Outline each blood parasite and name the species.
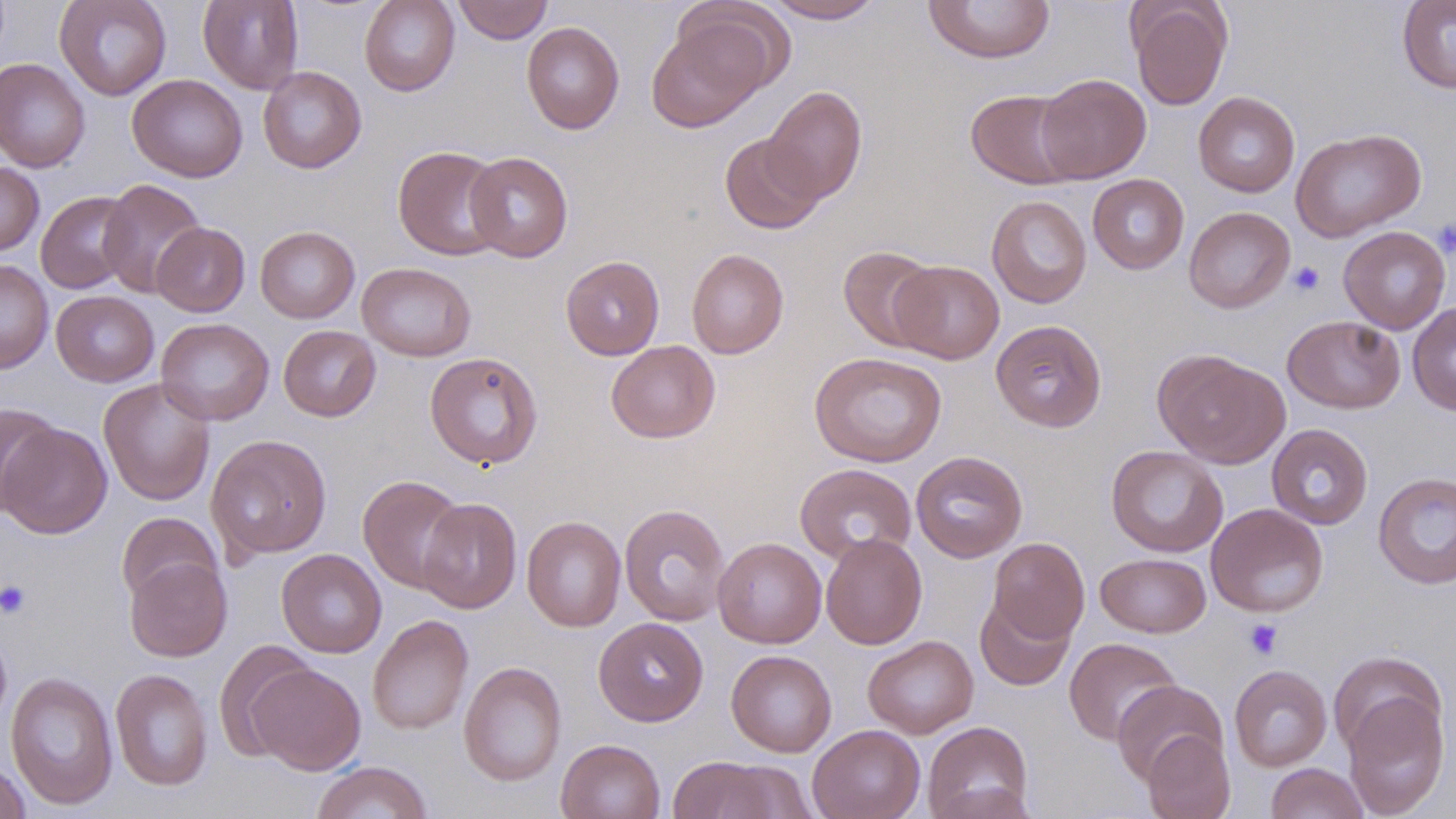
No blood parasites observed.

slide_level_diagnosis: no evidence of blood parasites
uninfected_red_blood_cell_locations: 'approximate bounding boxes as (x1,y1)-(x2,y2) corner pairs in pixels: (54,0)-(172,101), (198,0)-(304,94), (359,0)-(460,96), (453,0)-(553,44), (763,0)-(886,23), (1128,0)-(1233,110), (922,1)-(1055,65), (1397,1)-(1456,93), (646,18)-(770,132), (521,22)-(624,134), (0,58)-(90,173), (258,66)-(367,173), (127,74)-(247,182), (1035,74)-(1151,183), (762,85)-(867,204), (965,88)-(1083,189), (1193,91)-(1300,197), (1290,128)-(1426,242), (720,133)-(826,234), (392,145)-(507,261), (465,151)-(573,263), (0,161)-(44,256), (1088,174)-(1189,274), (98,179)-(206,298), (36,191)-(136,294), (986,195)-(1092,308), (1184,206)-(1295,313), (151,222)-(250,317), (255,226)-(360,323), (1338,226)-(1451,334), (838,246)-(940,352), (687,249)-(788,358), (561,255)-(664,360), (0,260)-(53,374), (890,260)-(1004,364), (357,262)-(475,361), (51,290)-(159,387), (1407,302)-(1456,416), (1282,316)-(1405,413), (155,318)-(274,425), (990,319)-(1107,432), (278,325)-(381,422), (606,340)-(720,443), (1153,349)-(1290,468), (809,351)-(947,467), (424,352)-(543,469), (99,378)-(216,506), (1,401)-(61,516), (1,422)-(112,539), (1266,424)-(1373,529), (206,434)-(332,560), (1105,445)-(1228,557), (910,451)-(1027,563), (795,463)-(916,565), (1372,472)-(1456,589), (357,474)-(468,594), (417,497)-(522,614), (619,503)-(730,626), (1206,503)-(1329,617), (116,512)-(222,606), (521,515)-(626,632), (821,533)-(926,649), (712,537)-(826,648), (988,537)-(1090,643), (276,549)-(387,658), (1096,552)-(1211,638), (125,556)-(232,662), (975,594)-(1076,692), (367,614)-(473,735), (593,617)-(708,726), (0,624)-(12,735), (862,635)-(978,738), (1064,637)-(1181,745), (214,641)-(316,761), (726,650)-(837,757), (1328,650)-(1447,759), (458,661)-(567,787), (248,662)-(366,774), (1229,665)-(1332,771), (111,668)-(213,791), (6,671)-(119,810), (1111,679)-(1228,785), (1342,689)-(1450,818), (922,721)-(1033,819), (807,724)-(925,819), (1142,729)-(1235,819), (556,738)-(665,819), (667,755)-(789,819), (0,759)-(31,818), (310,761)-(433,819), (1265,763)-(1369,819)'
stain: May-Grünwald-Giemsa
preparation: thin blood film
platelet_locations: 'approximate bounding boxes as (x1,y1)-(x2,y2) corner pairs in pixels: (1432,217)-(1456,258), (1287,261)-(1325,297), (0,580)-(32,619), (1244,618)-(1283,659)'
modality: optical microscopy
image_size: 1456×819 pixels
field_of_view: one of a larger specimen
magnification: 1000x